Locate every Babesia divergens-infected red blood cell.
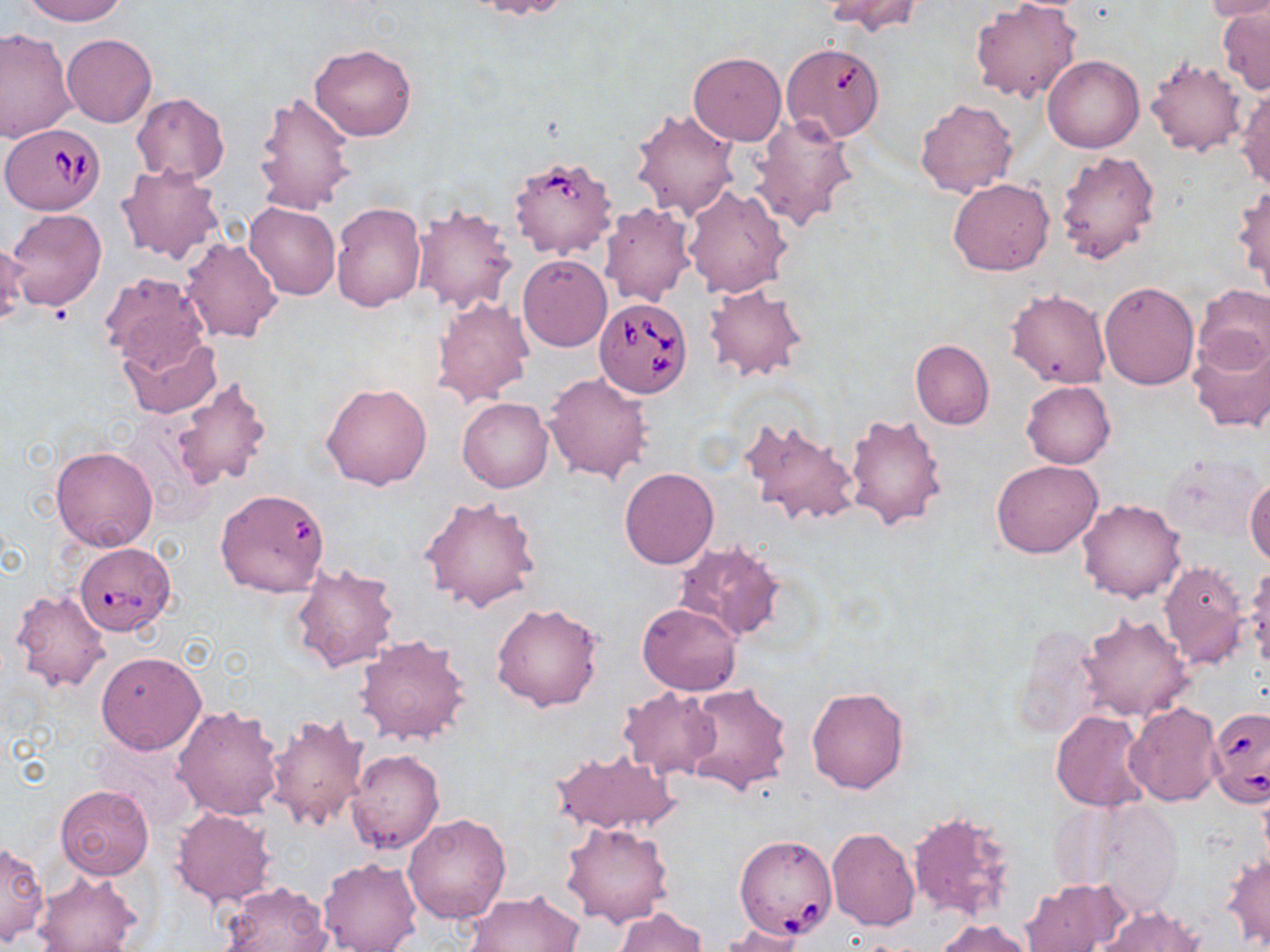
Approximate bounding boxes as (x1,y1)-(x2,y2) corner pairs in pixels.
Babesia divergens-infected red blood cells: (2,123)-(106,214), (509,152)-(619,259), (594,297)-(693,398), (74,541)-(175,635), (1207,706)-(1269,808), (734,834)-(837,939).

Uninfected red blood cell locations: (17,0)-(127,26), (467,0)-(572,20), (824,0)-(926,35), (970,1)-(1083,104), (1204,1)-(1270,23), (1216,7)-(1270,94), (0,29)-(77,141), (62,33)-(157,127), (309,43)-(417,141), (689,52)-(787,146), (1042,54)-(1143,153), (1145,55)-(1248,157), (1234,83)-(1270,191), (254,91)-(356,213), (131,92)-(230,184), (914,98)-(1018,200), (630,108)-(740,220), (751,113)-(860,230), (1055,150)-(1160,264), (115,163)-(226,267), (948,177)-(1054,275), (1232,182)-(1269,292), (682,184)-(792,299), (245,202)-(340,300), (330,202)-(426,312), (598,202)-(695,306), (412,204)-(520,316), (6,208)-(106,312), (180,237)-(282,343), (1,238)-(28,324), (518,255)-(612,352), (99,273)-(211,373), (1099,281)-(1198,390), (703,283)-(808,382), (1192,284)-(1270,374), (1006,289)-(1109,389), (433,295)-(534,408), (119,328)-(221,418), (1188,334)-(1270,433), (910,338)-(993,430), (543,371)-(651,481), (170,376)-(273,491), (1022,380)-(1115,469), (321,381)-(432,491), (457,398)-(552,493), (845,410)-(948,531), (738,417)-(861,530), (50,445)-(158,552), (1163,454)-(1262,543), (991,460)-(1102,556), (620,468)-(718,569), (1246,473)-(1270,566), (420,494)-(542,612), (212,495)-(330,605), (1077,498)-(1187,603), (672,538)-(786,643), (289,561)-(400,672), (1157,561)-(1249,669), (1243,561)-(1270,675), (9,589)-(110,694), (490,602)-(603,713), (637,602)-(741,695), (1075,611)-(1195,722), (1006,625)-(1105,742), (355,634)-(471,746), (96,651)-(207,754), (682,683)-(791,794), (618,686)-(723,781), (805,686)-(909,794), (1124,702)-(1222,806), (171,705)-(285,821), (264,710)-(368,832), (1050,710)-(1153,812), (95,736)-(194,827), (550,747)-(681,836), (344,748)-(444,856), (55,783)-(154,880), (1073,797)-(1188,917), (171,808)-(275,907), (908,809)-(1017,924), (404,812)-(511,925), (561,821)-(674,928), (825,828)-(921,931), (1,840)-(48,944), (1222,850)-(1270,950), (317,855)-(422,952), (32,871)-(143,952), (1020,879)-(1121,952), (220,881)-(333,952), (465,890)-(585,951), (1099,904)-(1207,950), (614,907)-(707,952), (935,919)-(1035,952), (718,924)-(809,951). Slide-level diagnosis: Babesia divergens. Image is 1270×952 pixels. Light microscopy. Thin blood smear. Single field of view. Captured at 1000x magnification. May-Grünwald-Giemsa stain.